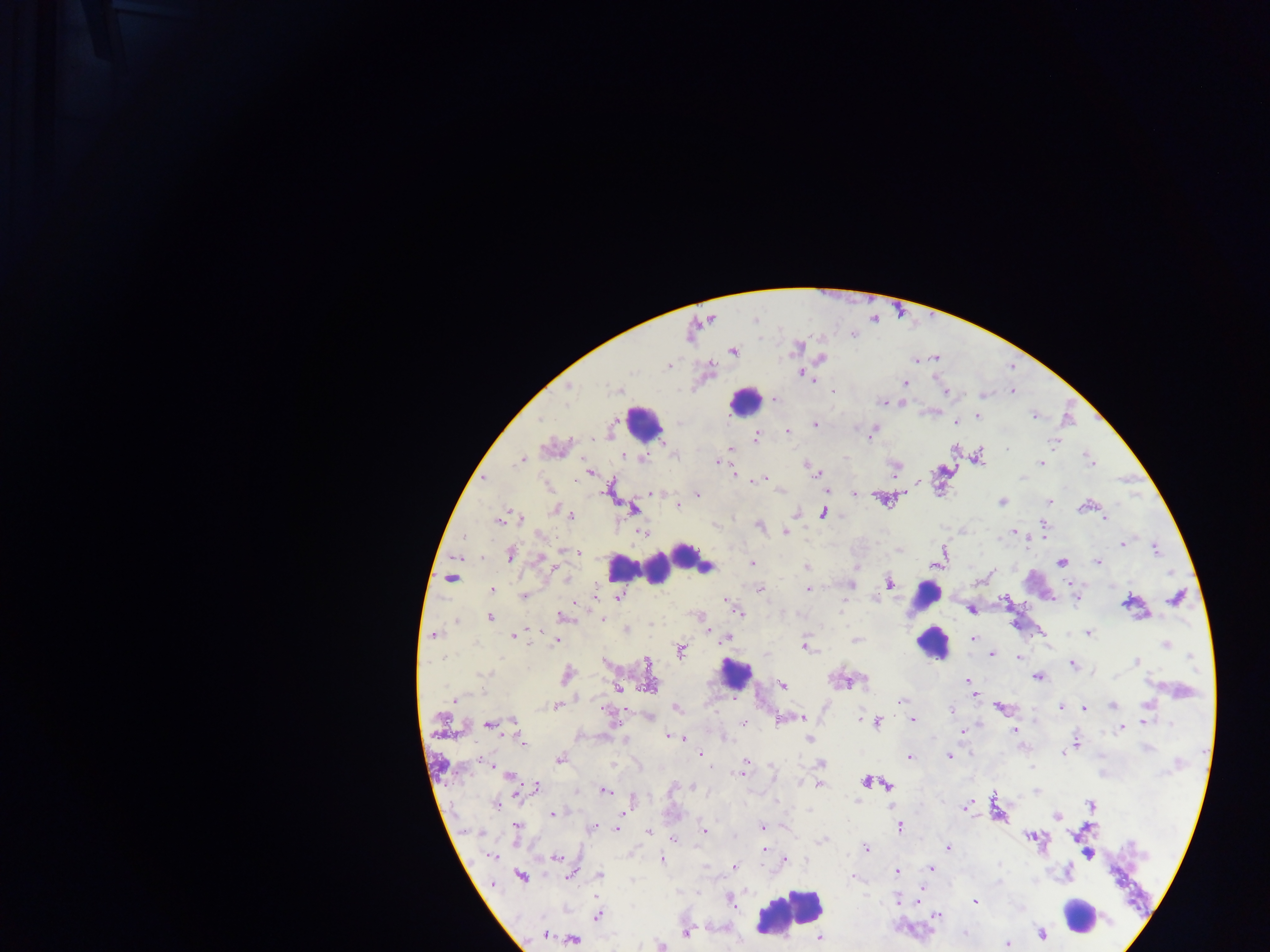
Approximate centers as [x, y] in pixels.
Summary:
  - Malaria parasite locations: [853, 335], [733, 350], [822, 358], [933, 358], [916, 360], [801, 373], [905, 383], [568, 386], [620, 390], [832, 391], [1012, 392], [946, 393], [982, 395], [773, 399], [901, 401], [884, 402], [977, 415], [1035, 415], [954, 422], [813, 424], [872, 431], [788, 432], [755, 436], [1054, 440], [553, 448], [730, 449], [623, 456], [975, 457], [523, 458], [641, 458], [717, 462], [1090, 463], [1041, 464], [805, 465], [894, 466], [590, 472], [733, 473], [817, 473], [484, 478], [762, 479], [825, 490], [649, 493], [854, 493], [697, 495], [882, 497], [1001, 502], [1049, 502], [677, 505], [1087, 505], [556, 508], [633, 509], [561, 511], [795, 512], [822, 512], [570, 515], [1105, 518], [501, 519], [520, 519], [759, 525], [1043, 530], [644, 532], [784, 532], [1014, 532], [1123, 543], [1155, 548], [578, 552], [510, 553], [943, 554], [541, 559], [1097, 561], [1061, 562], [752, 563], [936, 564], [806, 568], [452, 576], [889, 583], [851, 585], [758, 588], [492, 590], [808, 590], [524, 596], [618, 596], [1076, 598], [1176, 598], [726, 600], [1005, 600], [1131, 603], [971, 609], [740, 614], [699, 615], [489, 617], [562, 617], [709, 630], [1087, 633], [434, 635], [513, 636], [727, 638], [973, 638], [556, 640], [1165, 645], [804, 646], [680, 649], [992, 654], [1019, 657], [1136, 662], [1072, 664], [566, 675], [1036, 676], [968, 679], [845, 680], [782, 684], [649, 685], [618, 687], [971, 694], [454, 700], [901, 701], [557, 706], [1111, 706], [1000, 707], [1062, 707], [677, 708], [1083, 708], [952, 711], [650, 717], [802, 717], [781, 719], [511, 720], [912, 720], [1143, 721], [876, 722], [744, 723], [489, 725], [1121, 728], [962, 731], [1014, 731], [668, 736], [683, 738], [521, 740], [809, 740], [1076, 745], [947, 755], [907, 756], [560, 759], [485, 761], [706, 762], [745, 764], [821, 764], [614, 766], [709, 766], [741, 771], [509, 775], [866, 781], [819, 783], [871, 783], [887, 785], [535, 786], [693, 788], [605, 790], [496, 805], [1091, 805], [966, 806], [622, 811], [997, 811], [553, 814], [1058, 816], [899, 825], [516, 827], [592, 828], [762, 828], [617, 829], [648, 831], [704, 831], [1031, 836], [673, 839], [948, 847], [866, 849], [765, 850], [1088, 854], [490, 856], [555, 857], [661, 860], [784, 861], [733, 867], [929, 868], [896, 871], [570, 874], [520, 875], [599, 875], [853, 877], [493, 885], [898, 899], [729, 900], [918, 901], [973, 901], [597, 915], [936, 916], [687, 931], [964, 933], [1041, 933], [544, 934], [572, 938], [820, 938], [1006, 943], [661, 945]
  - Leukocyte locations: [743, 401], [644, 423], [700, 561], [626, 567], [652, 567], [925, 595], [932, 643], [736, 674], [791, 910], [1079, 915]
  - Capture: mobile-phone photograph through a microscope
  - Field of view: single
  - Image size: 1270×952 pixels
  - Country: Ghana
  - Preparation: thick blood smear